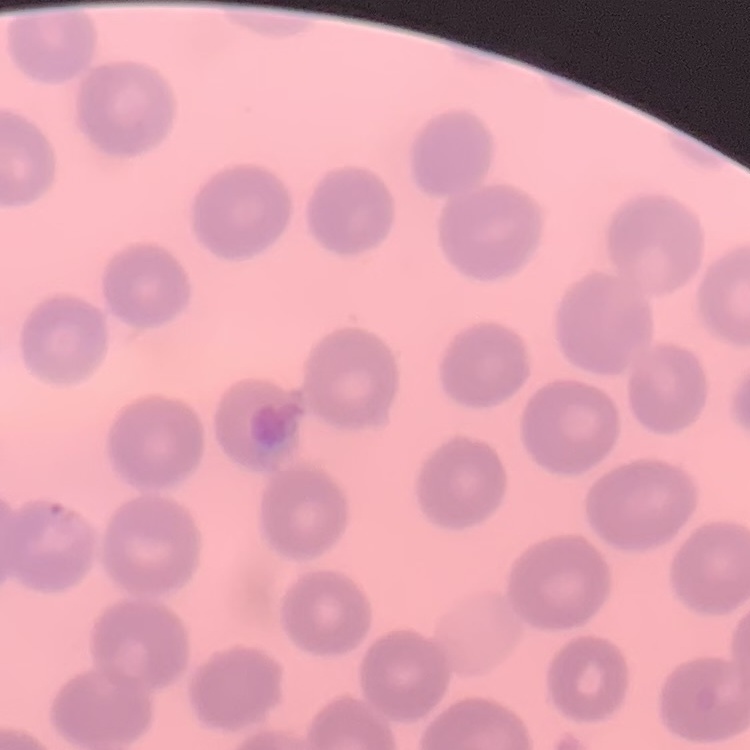 The erythrocytes show no rouleaux formation. Thin blood film. Field's or Giemsa stain. One tile cut from a larger photomicrograph.